Give the position of every leukocyte visible.
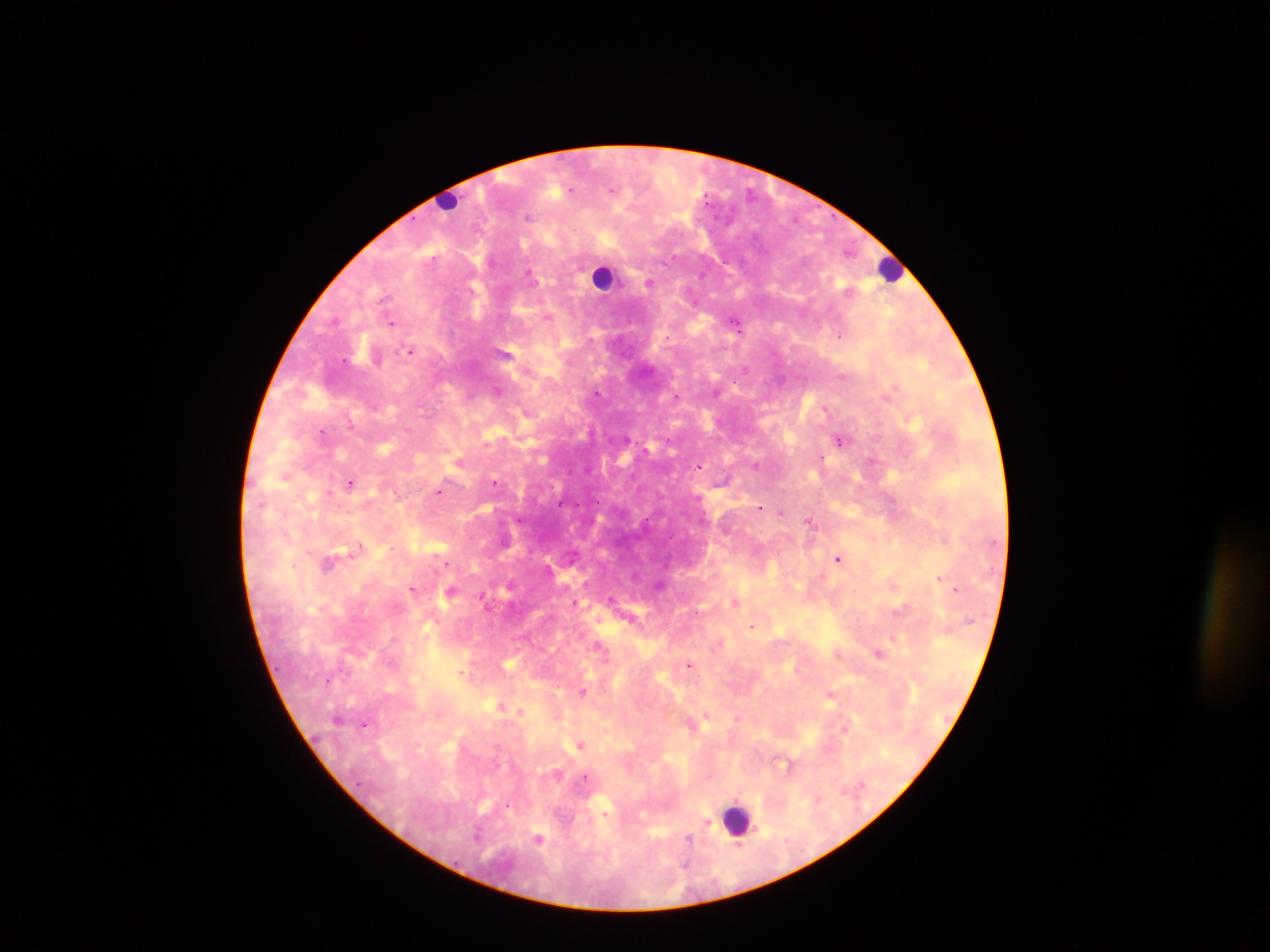

Approximate centers as {x, y} in pixels.
Leukocytes: {449, 203}, {892, 269}, {603, 277}, {737, 819}.

Malaria parasite locations: {570, 189}, {612, 190}, {528, 216}, {848, 251}, {673, 257}, {529, 273}, {649, 284}, {385, 298}, {391, 323}, {737, 326}, {839, 335}, {411, 350}, {344, 360}, {746, 369}, {497, 390}, {597, 393}, {676, 396}, {826, 409}, {350, 424}, {322, 431}, {839, 440}, {871, 461}, {756, 465}, {699, 466}, {284, 477}, {494, 482}, {350, 483}, {438, 491}, {396, 493}, {760, 507}, {780, 512}, {809, 521}, {359, 546}, {838, 558}, {328, 563}, {448, 564}, {939, 578}, {511, 583}, {412, 589}, {955, 589}, {451, 592}, {483, 597}, {612, 598}, {574, 602}, {735, 602}, {899, 610}, {752, 626}, {599, 645}, {879, 654}, {690, 664}, {461, 672}, {583, 693}, {831, 695}, {706, 715}, {737, 719}, {364, 725}, {580, 745}, {585, 777}, {507, 806}, {707, 823}, {478, 833}, {538, 839}, {689, 839}, {738, 846}, {686, 864}. Thick blood film. Photographed through a microscope with a mobile-phone camera. Image is 1270×952 pixels. Collected in Ghana. Single field of view.